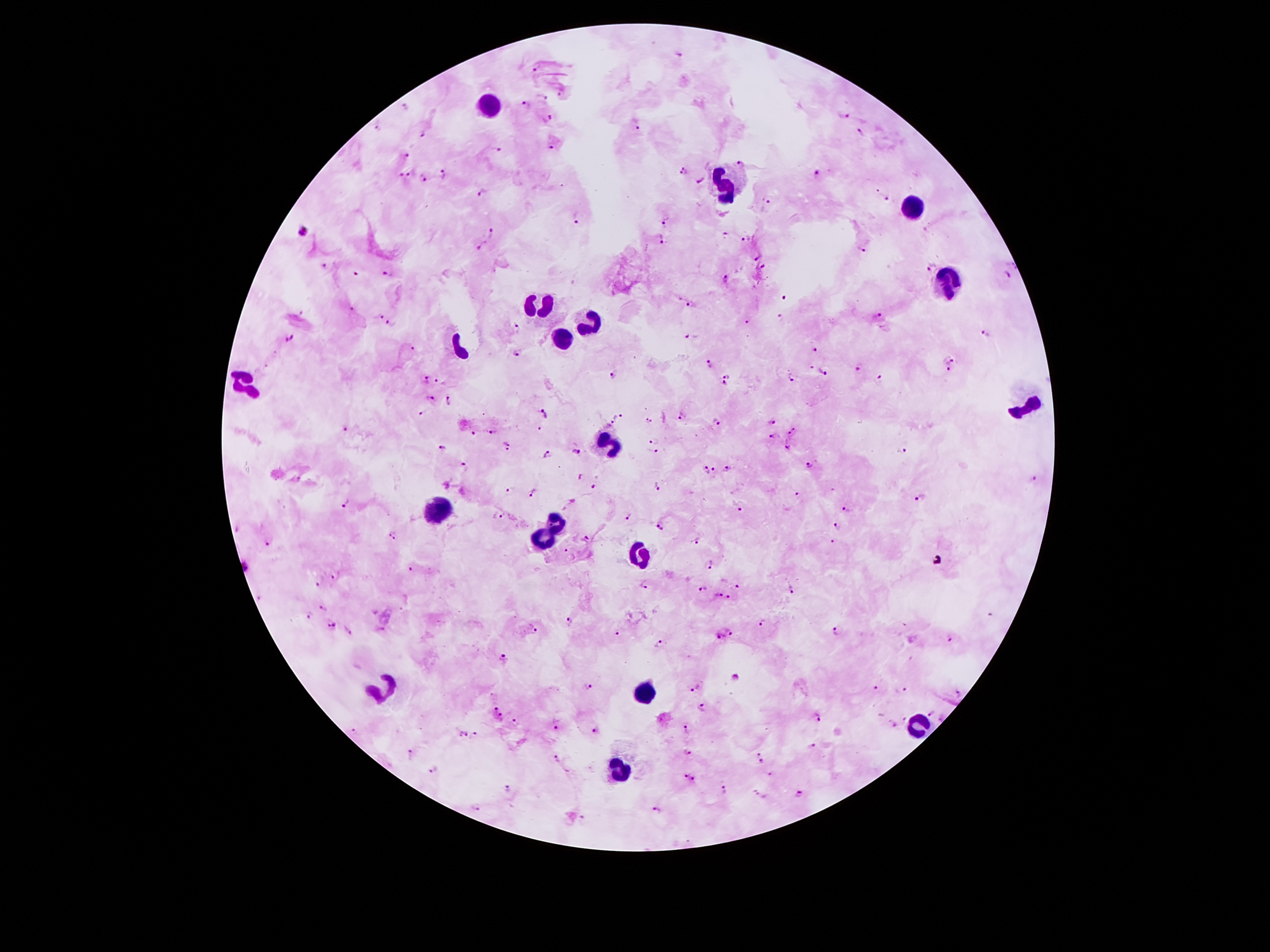
Approximate object centers, in pixels from the top-left corner. Plasmodium parasite locations: (x=679, y=53), (x=533, y=70), (x=546, y=98), (x=527, y=103), (x=844, y=116), (x=547, y=118), (x=637, y=128), (x=376, y=129), (x=860, y=132), (x=424, y=134), (x=551, y=147), (x=495, y=149), (x=405, y=155), (x=740, y=161), (x=683, y=170), (x=817, y=171), (x=444, y=173), (x=401, y=174), (x=409, y=175), (x=425, y=178), (x=702, y=178), (x=483, y=192), (x=769, y=199), (x=888, y=199), (x=577, y=216), (x=664, y=222), (x=304, y=232), (x=492, y=232), (x=723, y=234), (x=746, y=237), (x=662, y=239), (x=483, y=245), (x=861, y=250), (x=756, y=256), (x=765, y=265), (x=930, y=265), (x=1013, y=265), (x=325, y=266), (x=386, y=274), (x=355, y=275), (x=1004, y=276), (x=724, y=278), (x=784, y=296), (x=692, y=304), (x=351, y=309), (x=876, y=315), (x=780, y=317), (x=380, y=319), (x=746, y=322), (x=392, y=325), (x=515, y=327), (x=985, y=333), (x=690, y=335), (x=290, y=337), (x=412, y=348), (x=816, y=349), (x=518, y=352), (x=952, y=359), (x=709, y=364), (x=812, y=367), (x=858, y=367), (x=949, y=369), (x=822, y=370), (x=728, y=375), (x=615, y=376), (x=793, y=377), (x=880, y=378), (x=424, y=380), (x=440, y=380), (x=725, y=384), (x=431, y=398), (x=449, y=400), (x=545, y=411), (x=421, y=413), (x=681, y=415), (x=619, y=416), (x=648, y=420), (x=717, y=421), (x=771, y=422), (x=609, y=424), (x=539, y=429), (x=346, y=430), (x=492, y=432), (x=793, y=432), (x=474, y=433), (x=772, y=436), (x=656, y=439), (x=508, y=444), (x=787, y=447), (x=439, y=449), (x=574, y=451), (x=653, y=452), (x=904, y=452), (x=548, y=454), (x=464, y=466), (x=810, y=467), (x=728, y=468), (x=706, y=469), (x=714, y=471), (x=581, y=477), (x=297, y=478), (x=1035, y=479), (x=657, y=484), (x=596, y=486), (x=509, y=490), (x=532, y=495), (x=798, y=495), (x=919, y=498), (x=571, y=501), (x=346, y=504), (x=740, y=507), (x=850, y=511), (x=498, y=513), (x=626, y=517), (x=660, y=524), (x=836, y=527), (x=394, y=534), (x=588, y=537), (x=266, y=540), (x=696, y=541), (x=833, y=542), (x=566, y=551), (x=709, y=565), (x=410, y=569), (x=336, y=574), (x=318, y=585), (x=645, y=586), (x=736, y=586), (x=703, y=588), (x=792, y=588), (x=718, y=596), (x=729, y=597), (x=321, y=607), (x=310, y=615), (x=992, y=616), (x=570, y=621), (x=331, y=622), (x=762, y=623), (x=347, y=629), (x=377, y=630), (x=532, y=630), (x=731, y=631), (x=837, y=631), (x=617, y=633), (x=719, y=636), (x=952, y=637), (x=658, y=644), (x=504, y=660), (x=736, y=678), (x=588, y=687), (x=876, y=688), (x=696, y=689), (x=904, y=689), (x=958, y=693), (x=494, y=707), (x=702, y=707), (x=931, y=713), (x=500, y=717), (x=819, y=719), (x=904, y=719), (x=516, y=724), (x=895, y=725), (x=558, y=727), (x=687, y=729), (x=594, y=733), (x=464, y=734), (x=475, y=734), (x=812, y=746), (x=411, y=753), (x=687, y=753), (x=760, y=754), (x=558, y=757), (x=762, y=761), (x=434, y=769), (x=771, y=773), (x=686, y=778), (x=695, y=779), (x=509, y=789), (x=726, y=789), (x=756, y=793), (x=801, y=794), (x=477, y=806), (x=657, y=810), (x=581, y=818). Leukocyte locations: (x=489, y=104), (x=724, y=184), (x=912, y=205), (x=949, y=283), (x=538, y=306), (x=591, y=324), (x=562, y=338), (x=246, y=385), (x=1027, y=405), (x=606, y=445), (x=435, y=509), (x=556, y=521), (x=542, y=543), (x=635, y=555), (x=380, y=689), (x=643, y=692), (x=915, y=726), (x=622, y=772). Image is 1270×952 pixels. Patient malaria status: positive for Plasmodium falciparum. 100x magnification. Giemsa-stained preparation. Photographed through the microscope eyepiece with a smartphone camera. Thick peripheral-blood smear. Single field of view.